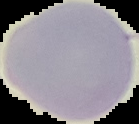
image size = 139×124 pixels
preparation = thin blood film
image type = segmented cell region on a black background
result = negative for malaria parasites